Locate every blood parasite and identify its species.
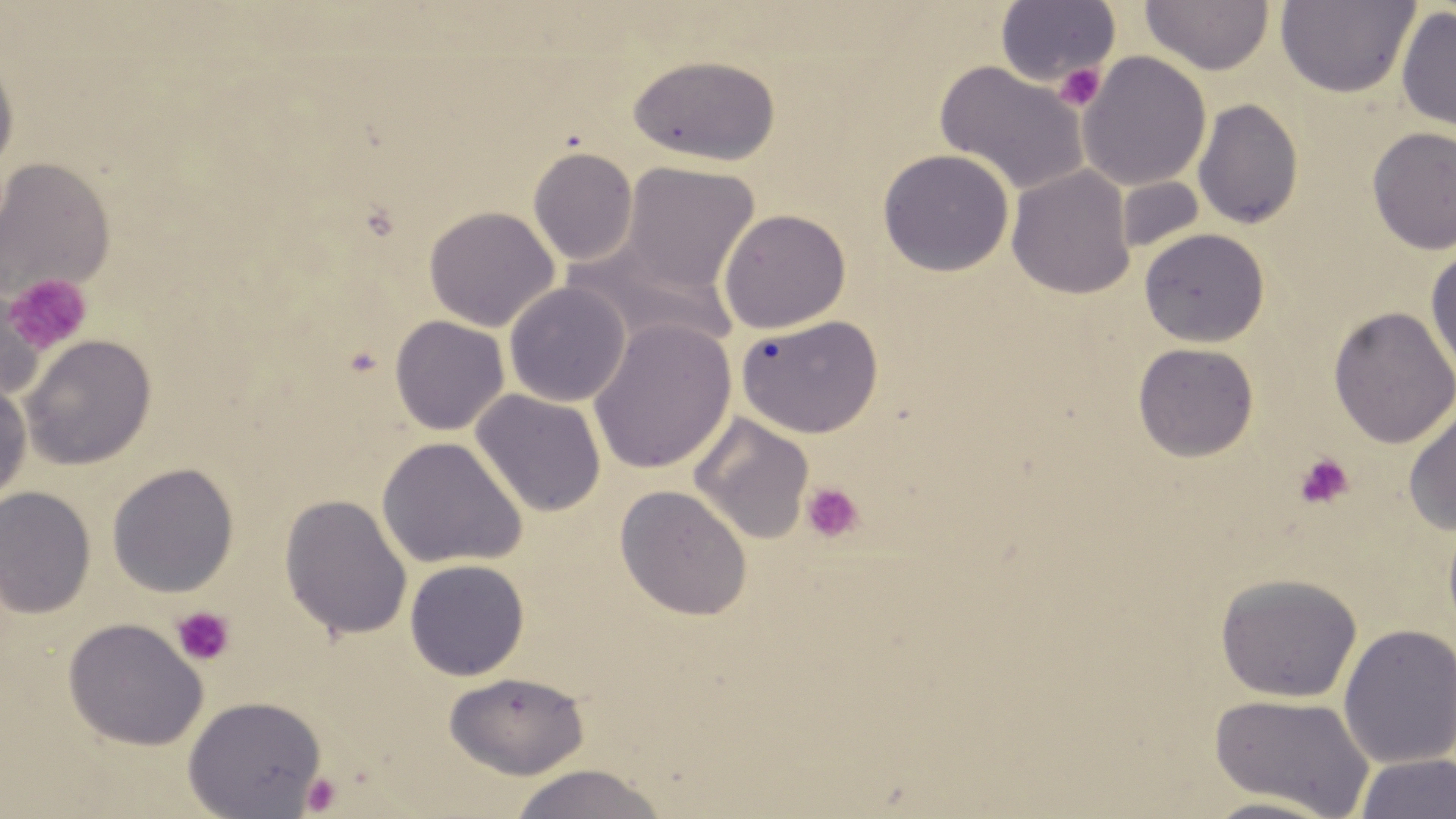
No blood parasites observed.

Summary:
  - Coordinate format: approximate bounding boxes as named x1/y1/x2/y2 corners in pixels
  - Uninfected red blood cell locations: (x1=1140, y1=0, x2=1274, y2=75), (x1=1274, y1=1, x2=1420, y2=99), (x1=996, y1=2, x2=1120, y2=87), (x1=1395, y1=6, x2=1456, y2=133), (x1=1077, y1=51, x2=1212, y2=192), (x1=626, y1=54, x2=782, y2=166), (x1=0, y1=55, x2=19, y2=175), (x1=933, y1=60, x2=1089, y2=197), (x1=1192, y1=98, x2=1305, y2=229), (x1=1366, y1=126, x2=1456, y2=255), (x1=527, y1=146, x2=639, y2=265), (x1=877, y1=148, x2=1014, y2=277), (x1=0, y1=157, x2=115, y2=302), (x1=619, y1=162, x2=760, y2=297), (x1=1006, y1=165, x2=1136, y2=299), (x1=1115, y1=176, x2=1206, y2=256), (x1=423, y1=205, x2=559, y2=332), (x1=718, y1=208, x2=851, y2=334), (x1=1138, y1=227, x2=1270, y2=347), (x1=567, y1=241, x2=738, y2=354), (x1=1425, y1=245, x2=1456, y2=382), (x1=503, y1=282, x2=630, y2=407), (x1=0, y1=287, x2=45, y2=406), (x1=1328, y1=306, x2=1456, y2=449), (x1=735, y1=314, x2=883, y2=438), (x1=388, y1=315, x2=509, y2=435), (x1=587, y1=317, x2=736, y2=475), (x1=20, y1=334, x2=157, y2=470), (x1=1132, y1=342, x2=1259, y2=462), (x1=0, y1=375, x2=32, y2=511), (x1=470, y1=389, x2=607, y2=518), (x1=1403, y1=401, x2=1456, y2=535), (x1=688, y1=412, x2=815, y2=544), (x1=376, y1=436, x2=528, y2=570), (x1=106, y1=462, x2=240, y2=597), (x1=615, y1=484, x2=753, y2=621), (x1=0, y1=486, x2=96, y2=618), (x1=278, y1=493, x2=413, y2=641), (x1=404, y1=559, x2=530, y2=680), (x1=1215, y1=572, x2=1363, y2=703), (x1=62, y1=617, x2=208, y2=751), (x1=1338, y1=623, x2=1456, y2=768), (x1=443, y1=670, x2=590, y2=780), (x1=1208, y1=692, x2=1375, y2=817), (x1=182, y1=695, x2=327, y2=818), (x1=1354, y1=753, x2=1455, y2=819), (x1=506, y1=763, x2=669, y2=819), (x1=1193, y1=795, x2=1343, y2=819)
  - Platelet locations: (x1=1053, y1=63, x2=1107, y2=111), (x1=3, y1=273, x2=93, y2=356), (x1=1294, y1=454, x2=1354, y2=509), (x1=801, y1=481, x2=864, y2=542), (x1=171, y1=606, x2=236, y2=667), (x1=301, y1=771, x2=343, y2=815)
  - Slide-level diagnosis: negative for blood parasites
  - Stain: May-Grünwald-Giemsa
  - Magnification: 1000x
  - Field of view: single
  - Preparation: thin blood smear
  - Image size: 1456×819 pixels
  - Modality: optical microscopy